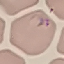
malaria status = parasitized
preparation = thin blood film
image type = automatically extracted cell patch, resized to 64 × 64 pixels
stain = Giemsa
capture = smartphone through the microscope eyepiece